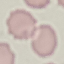

{
  "malaria_status": "uninfected",
  "capture": "smartphone camera at the microscope eyepiece",
  "preparation": "thin blood film",
  "image_type": "automatically extracted cell patch, resized to 64 × 64 pixels",
  "stain": "Giemsa"
}